Name the blood parasite species.
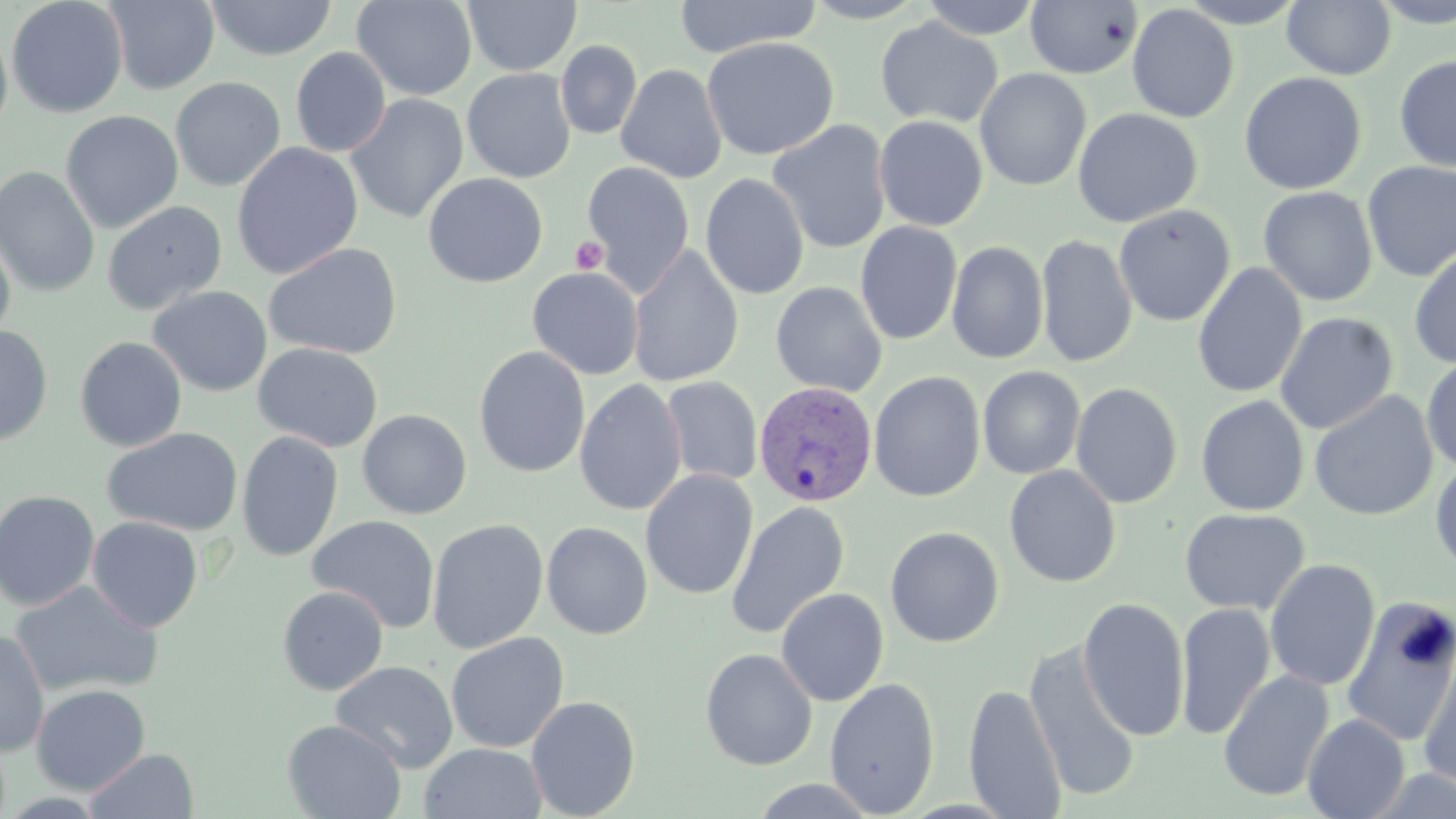

Plasmodium vivax.

field of view = one of a larger specimen
stain = May-Grünwald-Giemsa
uninfected red blood cell locations = approximate bounding boxes as (x1,y1)-(x2,y2) corner pairs in pixels: (5,0)-(129,118), (351,0)-(477,101), (672,0)-(821,58), (801,0)-(928,23), (918,0)-(1044,40), (1175,0)-(1309,28), (1371,0)-(1456,28), (103,1)-(220,94), (205,1)-(337,60), (463,1)-(582,76), (1025,1)-(1142,79), (1283,1)-(1396,80), (1126,4)-(1239,123), (875,16)-(1004,128), (0,18)-(13,144), (701,37)-(839,161), (556,40)-(642,139), (291,47)-(391,157), (1394,55)-(1456,174), (615,63)-(727,184), (461,68)-(576,183), (974,68)-(1091,191), (1239,72)-(1367,195), (170,77)-(286,192), (345,93)-(469,224), (1072,108)-(1202,227), (60,110)-(183,233), (874,115)-(988,231), (767,120)-(892,254), (231,142)-(363,280), (582,161)-(695,295), (1362,161)-(1456,281), (0,166)-(100,297), (422,172)-(549,288), (700,173)-(810,300), (1258,186)-(1378,306), (102,200)-(227,316), (1113,204)-(1236,327), (855,221)-(962,345), (0,228)-(16,347), (1036,234)-(1137,369), (946,241)-(1049,364), (264,242)-(403,360), (627,245)-(744,387), (1409,246)-(1456,370), (1192,262)-(1307,399), (527,267)-(644,380), (770,281)-(888,397), (148,285)-(272,397), (1274,311)-(1398,435), (0,325)-(53,446), (74,336)-(187,452), (253,342)-(383,453), (474,346)-(590,478), (1420,354)-(1456,474), (977,366)-(1085,479), (868,371)-(986,502), (660,376)-(763,486), (575,378)-(687,517), (1070,382)-(1183,509), (1308,389)-(1438,521), (1196,395)-(1310,516), (357,409)-(472,519), (102,427)-(243,536), (236,431)-(343,562), (1430,455)-(1456,578), (1004,465)-(1122,588), (640,469)-(758,600), (0,490)-(101,611), (725,500)-(850,640), (1179,508)-(1310,616), (307,515)-(440,633), (87,516)-(204,633), (427,518)-(548,654), (541,521)-(653,640), (885,526)-(1005,647), (1264,559)-(1380,692), (10,580)-(164,698), (277,586)-(389,696), (776,587)-(889,706), (1077,596)-(1190,741), (1341,596)-(1456,747), (1175,602)-(1276,740), (0,630)-(49,757), (445,632)-(569,753), (1023,641)-(1142,804), (700,648)-(818,770), (1418,649)-(1456,793), (331,660)-(459,773), (1218,669)-(1335,802), (824,677)-(940,817), (30,684)-(150,795), (963,684)-(1067,819), (526,695)-(640,818), (1302,713)-(1411,819), (282,719)-(407,819), (419,742)-(547,819), (84,748)-(199,818), (745,778)-(883,818)
modality = optical microscopy
Plasmodium vivax-infected red blood cell locations = approximate bounding boxes as (x1,y1)-(x2,y2) corner pairs in pixels: (753,381)-(879,508)
preparation = thin blood film
magnification = 1000x
image size = 1456×819 pixels
platelet locations = approximate bounding boxes as (x1,y1)-(x2,y2) corner pairs in pixels: (570,236)-(609,275)